Classify this cell by malaria status.
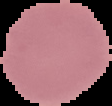
Uninfected.

The area outside the segmented cell region is set to black. Image is 112×106 pixels. From a thin blood film.